Name the cell type shown.
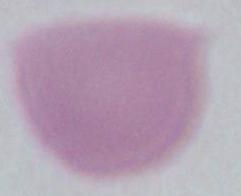
This is an erythrocyte.

{
  "magnification": "1000x",
  "modality": "micrograph"
}